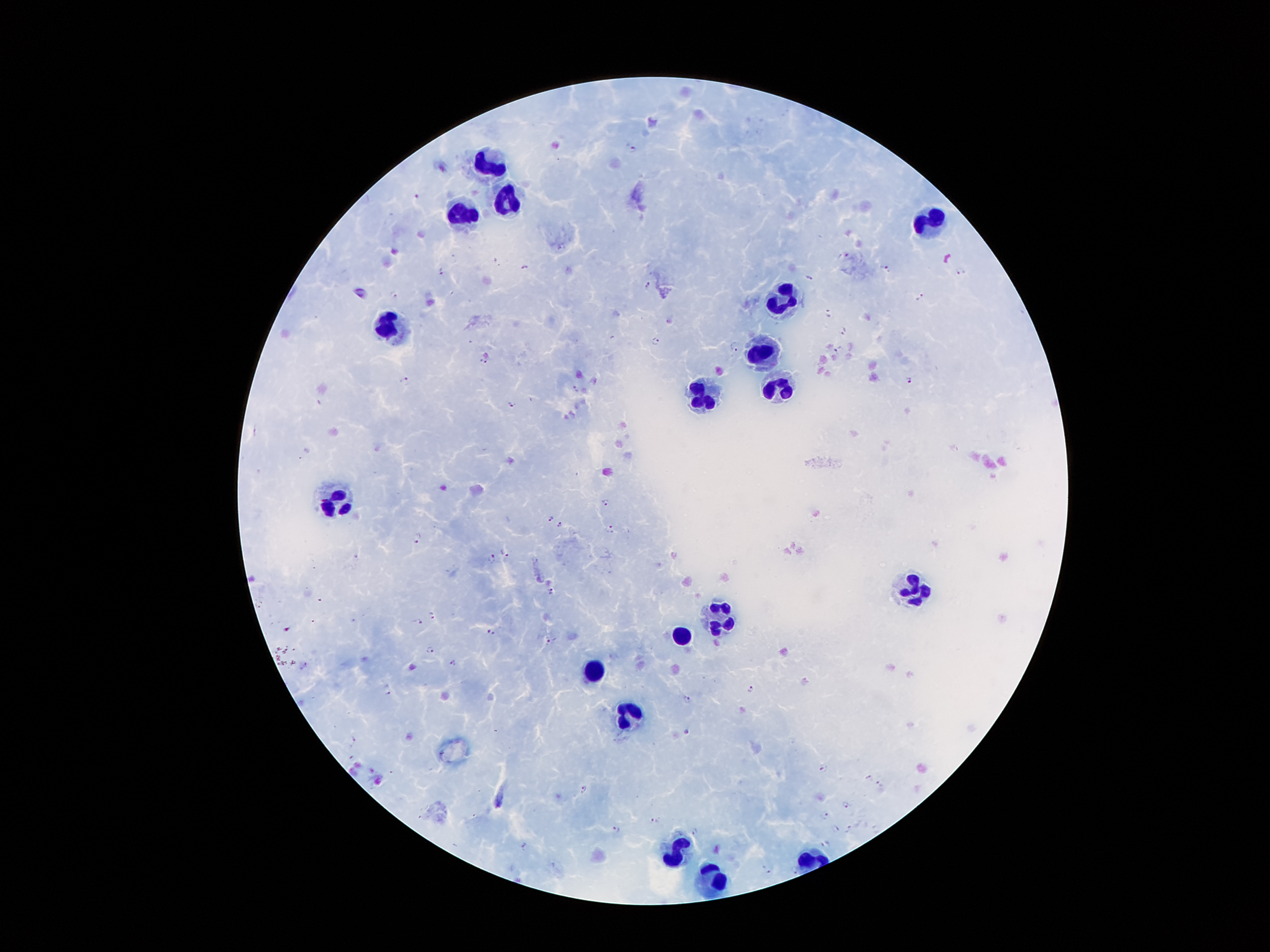

Approximate object centers, in pixels from the top-left corner. Malaria parasite locations: (x=632, y=148), (x=417, y=198), (x=845, y=256), (x=523, y=266), (x=885, y=268), (x=442, y=270), (x=960, y=270), (x=809, y=277), (x=647, y=284), (x=394, y=295), (x=921, y=296), (x=828, y=312), (x=844, y=329), (x=843, y=331), (x=656, y=341), (x=735, y=348), (x=837, y=348), (x=483, y=360), (x=404, y=380), (x=910, y=381), (x=576, y=388), (x=512, y=404), (x=605, y=502), (x=551, y=516), (x=560, y=524), (x=611, y=527), (x=417, y=538), (x=506, y=554), (x=492, y=558), (x=550, y=591), (x=259, y=605), (x=433, y=614), (x=418, y=621), (x=285, y=630), (x=491, y=633), (x=553, y=638), (x=430, y=649), (x=453, y=662), (x=304, y=665), (x=387, y=689), (x=751, y=690), (x=688, y=699), (x=687, y=732), (x=352, y=740), (x=824, y=770), (x=869, y=777), (x=878, y=783), (x=584, y=789), (x=845, y=802), (x=824, y=816), (x=654, y=820), (x=849, y=828), (x=875, y=828), (x=837, y=829), (x=616, y=830), (x=694, y=832), (x=824, y=845), (x=525, y=846), (x=766, y=869), (x=794, y=869), (x=795, y=869). Leukocyte locations: (x=488, y=166), (x=504, y=197), (x=460, y=214), (x=932, y=222), (x=785, y=299), (x=387, y=327), (x=760, y=355), (x=777, y=386), (x=700, y=396), (x=336, y=502), (x=912, y=586), (x=721, y=617), (x=683, y=637), (x=594, y=668), (x=633, y=714), (x=676, y=848), (x=713, y=878). Giemsa stain. Smartphone photograph taken through the microscope eyepiece. Image is 1270×952 pixels. Thick blood smear. 100x magnification. One field from this slide. Patient malaria status: positive for Plasmodium falciparum.